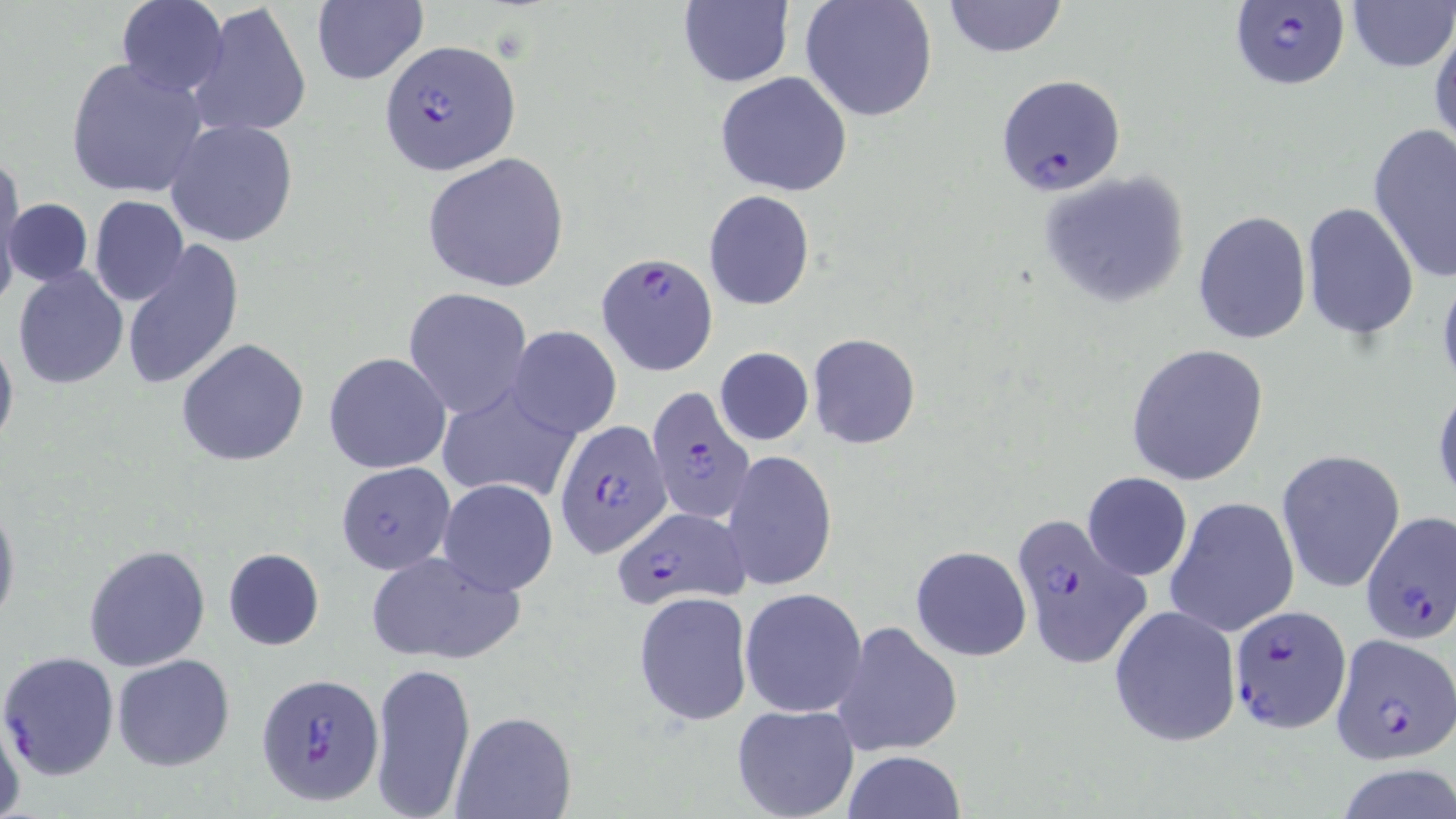

slide-level diagnosis = Plasmodium falciparum
uninfected red blood cell locations = approximate bounding boxes as named x1/y1/x2/y2 corners in pixels: (x1=116, y1=0, x2=228, y2=96), (x1=799, y1=0, x2=939, y2=123), (x1=941, y1=0, x2=1069, y2=57), (x1=1346, y1=0, x2=1453, y2=72), (x1=676, y1=1, x2=794, y2=88), (x1=186, y1=2, x2=311, y2=140), (x1=311, y1=2, x2=427, y2=85), (x1=1429, y1=16, x2=1456, y2=157), (x1=63, y1=56, x2=211, y2=199), (x1=716, y1=71, x2=852, y2=196), (x1=165, y1=119, x2=299, y2=247), (x1=1368, y1=125, x2=1456, y2=282), (x1=422, y1=152, x2=571, y2=293), (x1=0, y1=156, x2=23, y2=294), (x1=1037, y1=171, x2=1193, y2=311), (x1=704, y1=190, x2=815, y2=311), (x1=89, y1=196, x2=190, y2=307), (x1=5, y1=197, x2=93, y2=288), (x1=1300, y1=202, x2=1420, y2=341), (x1=1192, y1=209, x2=1311, y2=344), (x1=120, y1=238, x2=245, y2=392), (x1=1436, y1=263, x2=1456, y2=401), (x1=11, y1=265, x2=128, y2=389), (x1=402, y1=289, x2=532, y2=419), (x1=0, y1=324, x2=19, y2=455), (x1=507, y1=326, x2=622, y2=440), (x1=808, y1=334, x2=922, y2=449), (x1=176, y1=338, x2=311, y2=466), (x1=1125, y1=344, x2=1270, y2=487), (x1=715, y1=346, x2=813, y2=446), (x1=324, y1=352, x2=452, y2=474), (x1=1432, y1=379, x2=1456, y2=507), (x1=432, y1=384, x2=579, y2=506), (x1=723, y1=451, x2=837, y2=592), (x1=1276, y1=451, x2=1405, y2=594), (x1=337, y1=462, x2=456, y2=575), (x1=1080, y1=470, x2=1193, y2=582), (x1=438, y1=478, x2=559, y2=597), (x1=0, y1=495, x2=20, y2=634), (x1=1165, y1=496, x2=1300, y2=637), (x1=83, y1=544, x2=211, y2=671), (x1=910, y1=545, x2=1032, y2=663), (x1=222, y1=547, x2=325, y2=650), (x1=366, y1=550, x2=525, y2=667), (x1=740, y1=588, x2=868, y2=718), (x1=633, y1=591, x2=753, y2=727), (x1=1107, y1=604, x2=1241, y2=748), (x1=830, y1=620, x2=965, y2=756), (x1=0, y1=651, x2=120, y2=779), (x1=112, y1=653, x2=235, y2=771), (x1=370, y1=659, x2=476, y2=817), (x1=1, y1=702, x2=25, y2=818), (x1=731, y1=703, x2=860, y2=819), (x1=451, y1=711, x2=577, y2=819), (x1=842, y1=750, x2=964, y2=819), (x1=1333, y1=762, x2=1456, y2=819)
stain = May-Grünwald-Giemsa
field of view = one of a larger specimen
preparation = thin blood smear
Plasmodium falciparum-infected red blood cell locations = approximate bounding boxes as named x1/y1/x2/y2 corners in pixels: (x1=1230, y1=0, x2=1349, y2=89), (x1=379, y1=38, x2=520, y2=178), (x1=997, y1=74, x2=1126, y2=194), (x1=595, y1=252, x2=718, y2=376), (x1=646, y1=387, x2=755, y2=524), (x1=555, y1=420, x2=670, y2=560), (x1=1008, y1=509, x2=1150, y2=668), (x1=616, y1=511, x2=745, y2=610), (x1=1359, y1=512, x2=1456, y2=649), (x1=1227, y1=603, x2=1353, y2=733), (x1=1329, y1=634, x2=1454, y2=763), (x1=254, y1=671, x2=384, y2=806)
magnification = 1000x
modality = light microscopy
image size = 1456×819 pixels